Identify the cell.
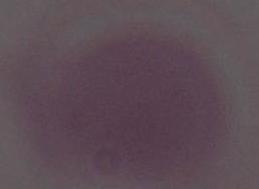

An erythrocyte.

Photomicrograph. 1000x magnification.